Give the extent of all uninfected red blood cells.
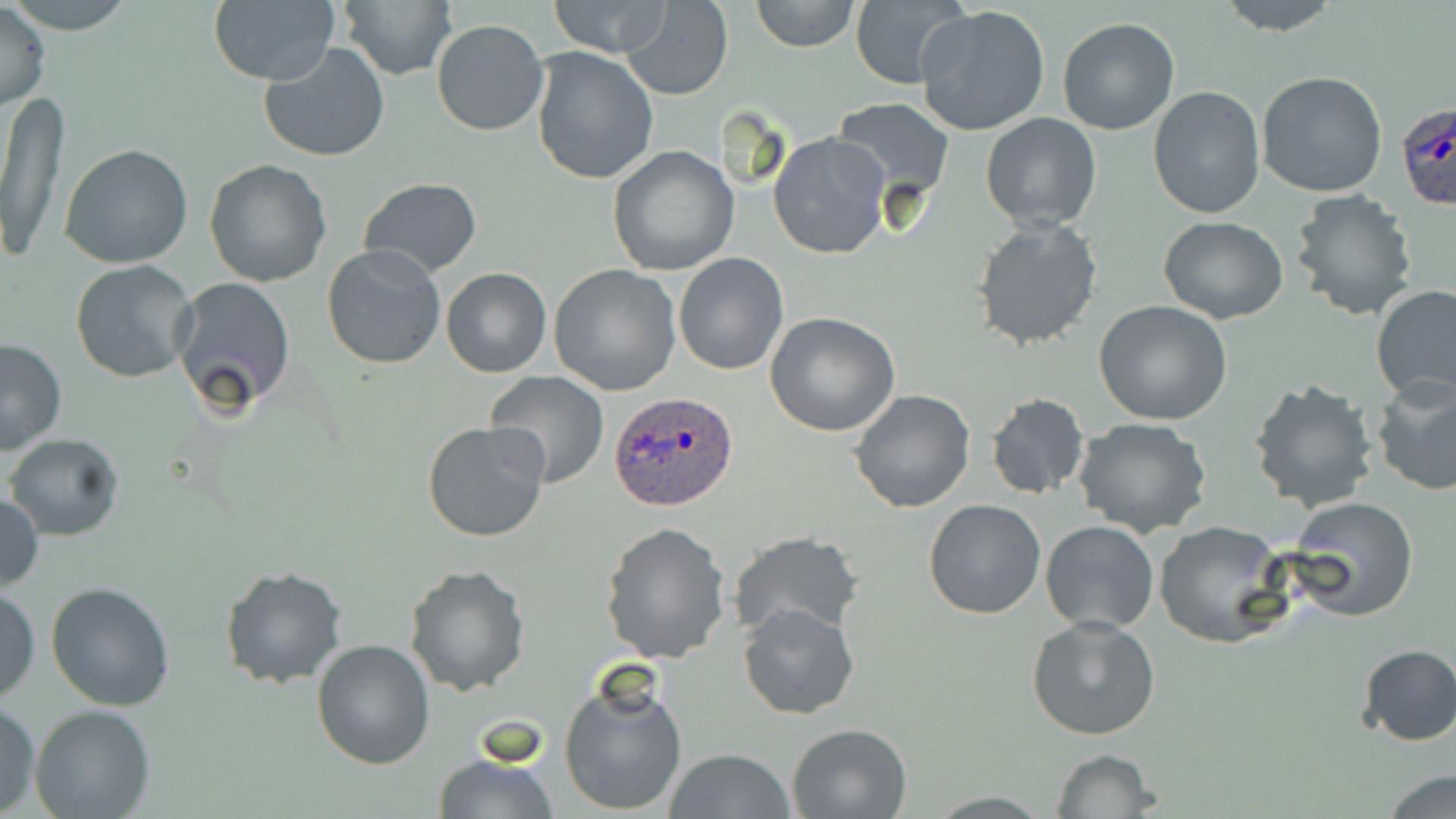

Approximate bounding boxes as named x1/y1/x2/y2 corners in pixels.
Uninfected red blood cells: (x1=2, y1=0, x2=141, y2=34), (x1=620, y1=0, x2=734, y2=101), (x1=749, y1=0, x2=859, y2=52), (x1=1211, y1=0, x2=1344, y2=36), (x1=0, y1=1, x2=50, y2=112), (x1=544, y1=1, x2=675, y2=58), (x1=207, y1=2, x2=340, y2=86), (x1=335, y1=2, x2=457, y2=81), (x1=848, y1=2, x2=967, y2=87), (x1=914, y1=5, x2=1052, y2=138), (x1=1057, y1=17, x2=1180, y2=136), (x1=431, y1=20, x2=549, y2=136), (x1=258, y1=43, x2=390, y2=163), (x1=529, y1=46, x2=659, y2=185), (x1=1257, y1=70, x2=1388, y2=196), (x1=1148, y1=86, x2=1266, y2=218), (x1=1, y1=91, x2=71, y2=263), (x1=830, y1=98, x2=956, y2=207), (x1=980, y1=113, x2=1103, y2=230), (x1=768, y1=133, x2=890, y2=259), (x1=60, y1=142, x2=194, y2=267), (x1=607, y1=146, x2=739, y2=276), (x1=203, y1=159, x2=332, y2=287), (x1=357, y1=177, x2=483, y2=278), (x1=1289, y1=189, x2=1420, y2=321), (x1=1158, y1=216, x2=1288, y2=323), (x1=971, y1=217, x2=1103, y2=352), (x1=321, y1=244, x2=449, y2=371), (x1=675, y1=252, x2=788, y2=376), (x1=69, y1=260, x2=199, y2=384), (x1=548, y1=264, x2=682, y2=395), (x1=440, y1=268, x2=551, y2=378), (x1=171, y1=276, x2=295, y2=414), (x1=1371, y1=285, x2=1456, y2=404), (x1=1094, y1=302, x2=1235, y2=426), (x1=766, y1=312, x2=900, y2=437), (x1=0, y1=337, x2=67, y2=455), (x1=484, y1=370, x2=609, y2=490), (x1=1247, y1=376, x2=1379, y2=513), (x1=1370, y1=377, x2=1456, y2=497), (x1=849, y1=388, x2=977, y2=513), (x1=984, y1=392, x2=1090, y2=499), (x1=1072, y1=418, x2=1214, y2=537), (x1=421, y1=420, x2=550, y2=543), (x1=6, y1=434, x2=125, y2=540), (x1=0, y1=490, x2=45, y2=594), (x1=1289, y1=497, x2=1420, y2=622), (x1=922, y1=498, x2=1048, y2=619), (x1=1041, y1=521, x2=1159, y2=633), (x1=1156, y1=521, x2=1291, y2=648), (x1=599, y1=522, x2=732, y2=666), (x1=726, y1=531, x2=863, y2=640), (x1=218, y1=564, x2=349, y2=688), (x1=402, y1=564, x2=531, y2=698), (x1=45, y1=581, x2=176, y2=712), (x1=1, y1=584, x2=41, y2=704), (x1=736, y1=602, x2=860, y2=720), (x1=1027, y1=614, x2=1161, y2=741), (x1=311, y1=639, x2=436, y2=771), (x1=1356, y1=644, x2=1456, y2=745), (x1=559, y1=679, x2=688, y2=815), (x1=0, y1=701, x2=42, y2=815), (x1=30, y1=706, x2=158, y2=819), (x1=787, y1=721, x2=914, y2=817), (x1=664, y1=748, x2=796, y2=819), (x1=1049, y1=749, x2=1162, y2=818), (x1=431, y1=751, x2=560, y2=819), (x1=1380, y1=769, x2=1456, y2=819).

Summary:
  - Plasmodium ovale-infected red blood cell locations: (x1=1396, y1=101, x2=1456, y2=212), (x1=609, y1=392, x2=738, y2=514)
  - Slide-level diagnosis: Plasmodium ovale
  - Field of view: one of a larger specimen
  - Stain: May-Grünwald-Giemsa
  - Image size: 1456×819 pixels
  - Modality: optical microscopy
  - Preparation: thin blood smear
  - Magnification: 1000x